Describe the morphology of the erythrocytes.
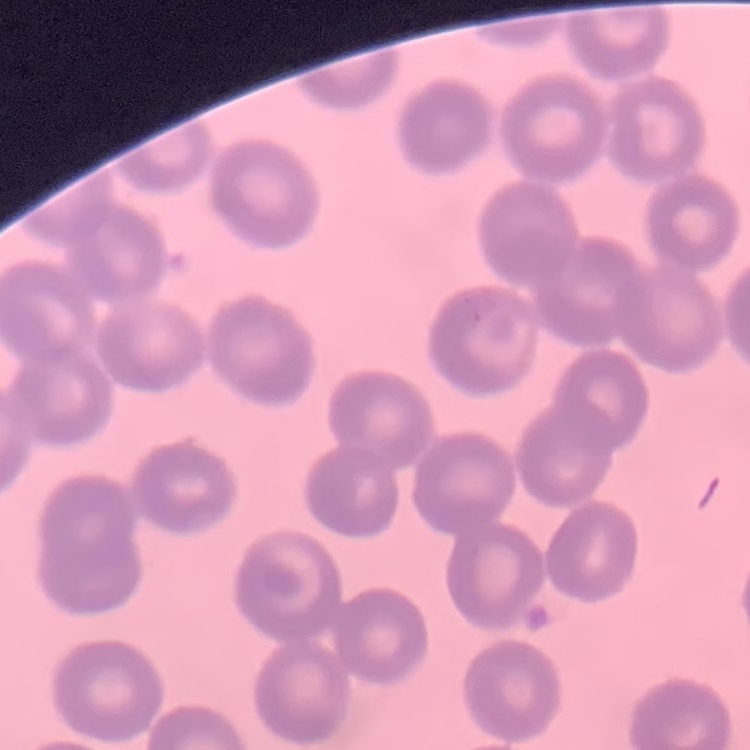

They show no rouleaux formation.

{
  "stain": "Field's or Giemsa",
  "image_type": "square crop of a larger photomicrograph",
  "preparation": "thin blood film"
}